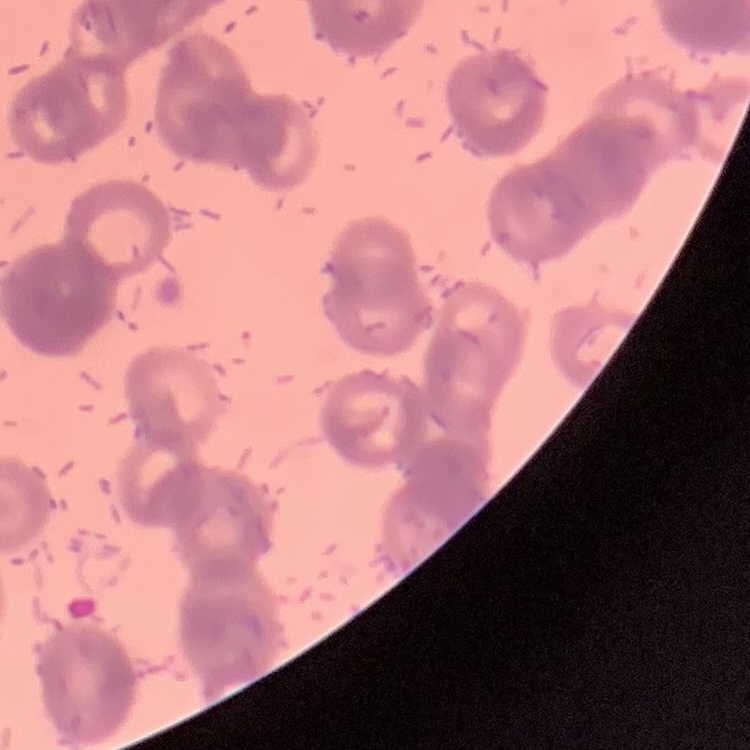
Summary:
  - Erythrocyte morphology: rouleaux formation
  - Preparation: thin blood film
  - Stain: Field's or Giemsa
  - Image type: square crop of a larger photomicrograph